Point out every Plasmodium parasite.
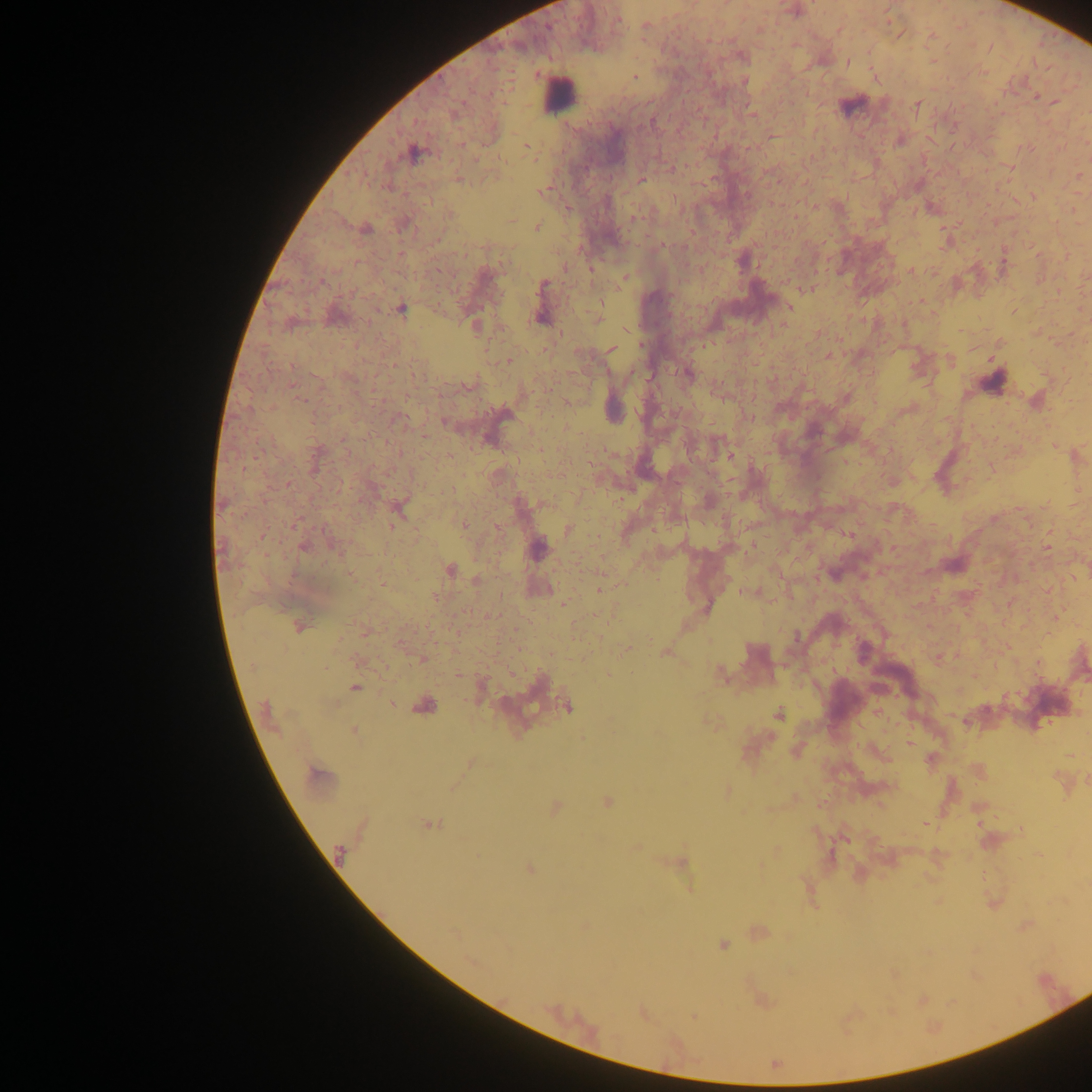
Approximate centers as {x, y} in pixels.
Plasmodium parasites: {647, 26}, {847, 62}, {635, 77}, {744, 82}, {1036, 96}, {1054, 101}, {916, 106}, {751, 113}, {651, 123}, {526, 145}, {412, 153}, {459, 179}, {641, 180}, {541, 192}, {814, 206}, {636, 217}, {537, 227}, {366, 230}, {911, 270}, {624, 277}, {542, 285}, {810, 288}, {789, 308}, {401, 309}, {540, 318}, {598, 318}, {474, 325}, {611, 350}, {828, 355}, {508, 361}, {688, 374}, {469, 385}, {846, 397}, {301, 400}, {749, 417}, {445, 423}, {288, 484}, {295, 524}, {393, 524}, {464, 525}, {569, 530}, {1048, 547}, {538, 548}, {451, 569}, {351, 575}, {476, 580}, {599, 590}, {749, 592}, {299, 626}, {366, 632}, {796, 637}, {627, 648}, {755, 652}, {665, 653}, {422, 660}, {720, 674}, {356, 687}, {390, 703}, {425, 707}, {567, 707}, {778, 714}, {354, 731}, {909, 744}, {317, 776}, {607, 802}, {556, 808}, {429, 824}, {925, 824}, {340, 852}, {682, 862}, {529, 869}, {723, 945}, {693, 1016}, {775, 1064}.

Leukocyte locations: {557, 93}, {851, 105}, {993, 380}. Collected in Ghana. Image is 1092×1092 pixels. Thick blood film. Photographed through a microscope with a mobile-phone camera. One field of view.